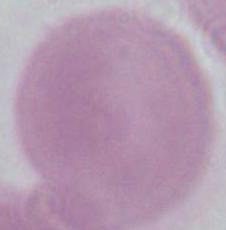

A red blood cell is seen. 1000x magnification. Photomicrograph.